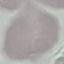

Malaria status: uninfected. Thin blood film. Acquired by smartphone through the microscope eyepiece. Giemsa stain. Cell patch, automatically extracted from a larger field of view and resized to 64 × 64 pixels.